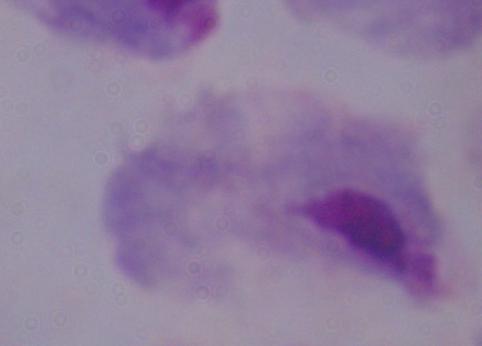

{
  "magnification": "1000x",
  "identification": "trichomonad",
  "modality": "photomicrograph"
}